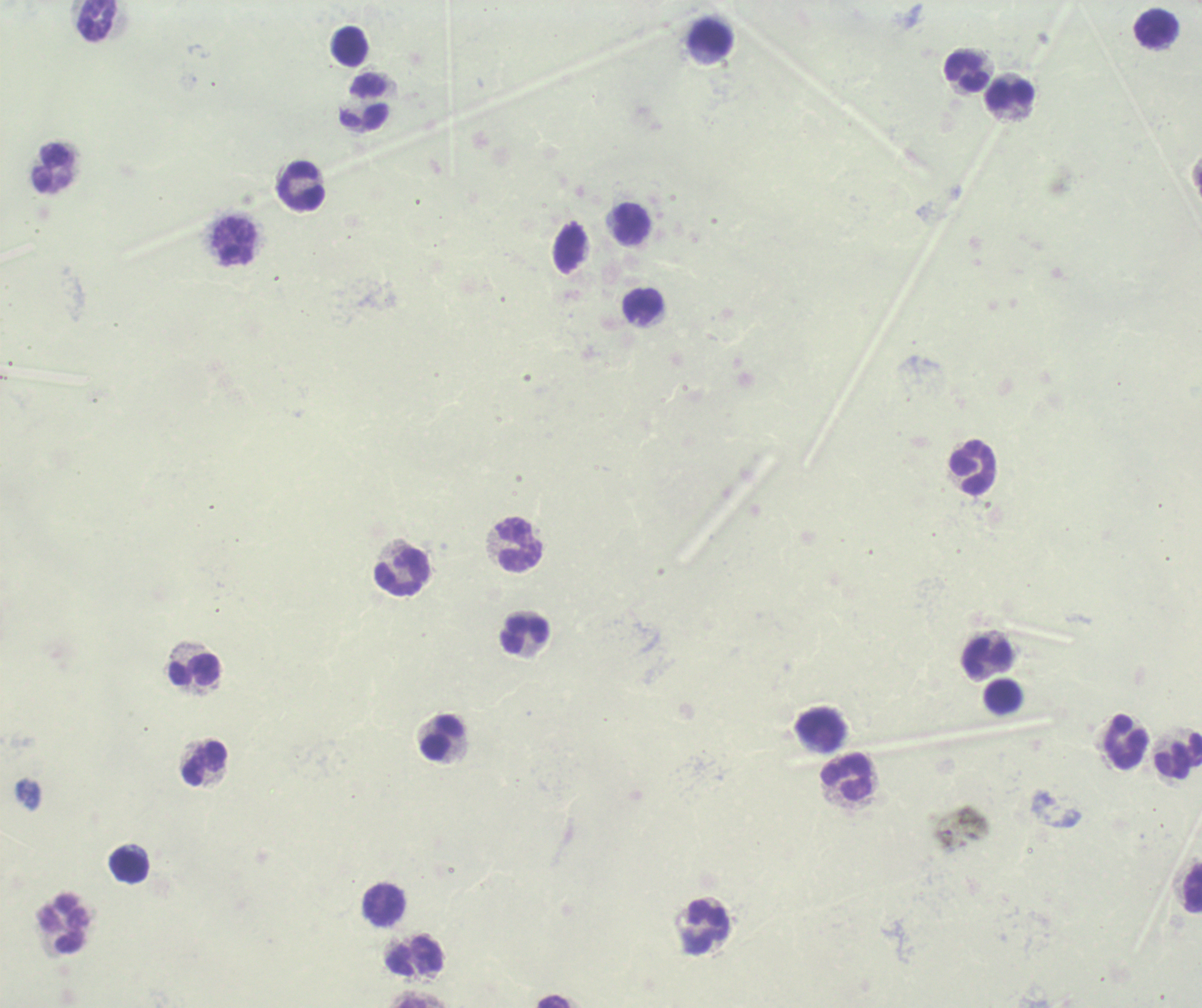

Approximate centers as [x, y] in pixels.
Summary:
  - Leukocyte locations: [96, 20], [1156, 29], [711, 39], [350, 47], [966, 72], [1010, 94], [364, 103], [51, 169], [301, 187], [631, 223], [234, 242], [642, 307], [973, 468], [519, 545], [403, 573], [524, 635], [986, 654], [193, 670], [1003, 697], [821, 731], [442, 739], [1127, 742], [1178, 757], [205, 764], [847, 777], [128, 866], [1193, 888], [383, 906], [64, 925], [707, 929], [416, 957]
  - Background quality: unsatisfactory
  - Stain: Romanowsky
  - Field of view: one from this slide
  - Result: no Plasmodium parasites seen
  - Image size: 1202×1008 pixels
  - Context: previously used in a real diagnosis
  - Magnification: 100x
  - Preparation: thick smear of blood